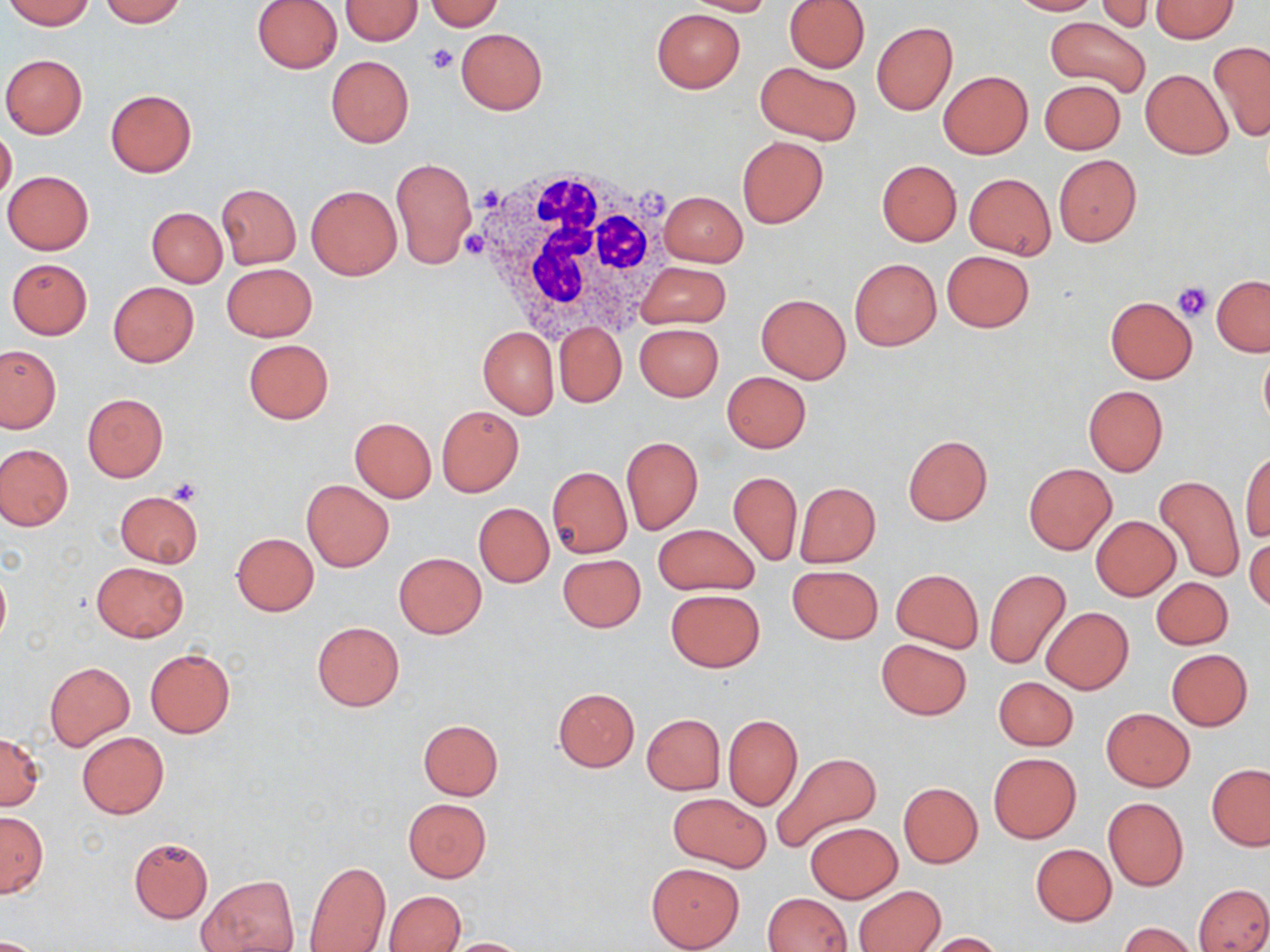

slide-level diagnosis = no evidence of blood parasites
preparation = thin blood smear
white blood cell locations = approximate bounding boxes as (x1,y1)-(x2,y2) corner pairs in pixels: (467,160)-(671,340)
modality = light microscopy
image size = 1270×952 pixels
uninfected red blood cell locations = approximate bounding boxes as (x1,y1)-(x2,y2) corner pairs in pixels: (3,0)-(95,29), (100,0)-(187,26), (251,0)-(342,74), (340,0)-(424,44), (685,0)-(776,16), (784,0)-(870,72), (1007,0)-(1099,15), (423,1)-(505,31), (1094,1)-(1155,33), (1151,1)-(1237,42), (651,8)-(745,93), (1044,18)-(1151,100), (871,21)-(958,115), (456,28)-(547,114), (1208,41)-(1270,142), (1,54)-(88,138), (325,55)-(414,147), (756,61)-(862,146), (1140,69)-(1232,160), (938,71)-(1032,159), (1040,80)-(1125,154), (105,88)-(196,176), (0,127)-(17,202), (737,135)-(828,228), (1053,154)-(1141,246), (392,157)-(478,269), (877,160)-(961,246), (964,166)-(1139,251), (3,170)-(94,254), (965,173)-(1055,260), (217,183)-(301,268), (306,184)-(402,280), (659,190)-(748,267), (146,207)-(227,287), (942,250)-(1034,333), (6,258)-(93,339), (849,258)-(941,351), (635,261)-(731,329), (222,263)-(317,341), (1212,275)-(1270,355), (108,281)-(199,367), (756,293)-(851,382), (1105,296)-(1197,383), (554,323)-(627,408), (634,324)-(724,402), (478,326)-(559,419), (243,339)-(333,424), (0,344)-(61,433), (1259,349)-(1270,432), (722,371)-(810,453), (1083,385)-(1168,476), (82,393)-(168,482), (436,406)-(524,497), (349,417)-(437,502), (903,435)-(993,525), (621,436)-(703,534), (1,443)-(72,530), (1241,449)-(1269,543), (1024,463)-(1117,556), (548,466)-(631,558), (728,470)-(802,567), (1153,474)-(1246,584), (301,480)-(393,571), (795,482)-(881,568), (116,491)-(203,568), (473,502)-(554,587), (1091,515)-(1180,600), (653,523)-(759,596), (1245,531)-(1269,615), (232,533)-(318,615), (394,552)-(486,638), (558,554)-(646,633), (92,562)-(188,641), (0,563)-(10,647), (787,565)-(883,643), (892,568)-(983,653), (984,568)-(1072,670), (1149,578)-(1234,651), (665,588)-(765,673), (1040,607)-(1133,694), (312,622)-(405,710), (877,638)-(972,720), (145,649)-(235,738), (1166,649)-(1253,730), (44,661)-(135,749), (993,676)-(1078,751), (552,687)-(640,771), (1101,708)-(1194,791), (641,714)-(726,795), (724,715)-(802,810), (418,719)-(503,800), (77,731)-(168,818), (0,733)-(44,809), (771,751)-(883,852), (988,752)-(1080,843), (1206,763)-(1270,849), (898,782)-(983,867), (668,792)-(771,872), (403,798)-(491,882), (1103,798)-(1188,891), (0,812)-(47,898), (804,821)-(903,903), (129,835)-(213,923), (1030,844)-(1117,926), (304,860)-(391,952), (646,863)-(744,951), (198,876)-(298,951), (1194,883)-(1270,951), (854,885)-(944,952), (385,890)-(466,952), (763,893)-(852,952), (1120,922)-(1198,952), (921,932)-(1005,951), (443,937)-(531,951)
field of view = one of a larger specimen
magnification = 1000x
platelet locations = approximate bounding boxes as (x1,y1)-(x2,y2) corner pairs in pixels: (425,43)-(458,75), (481,188)-(501,210), (462,226)-(489,261), (1174,283)-(1211,321), (170,478)-(203,505)
stain = May-Grünwald-Giemsa